Locate every blood parasite and identify its species.
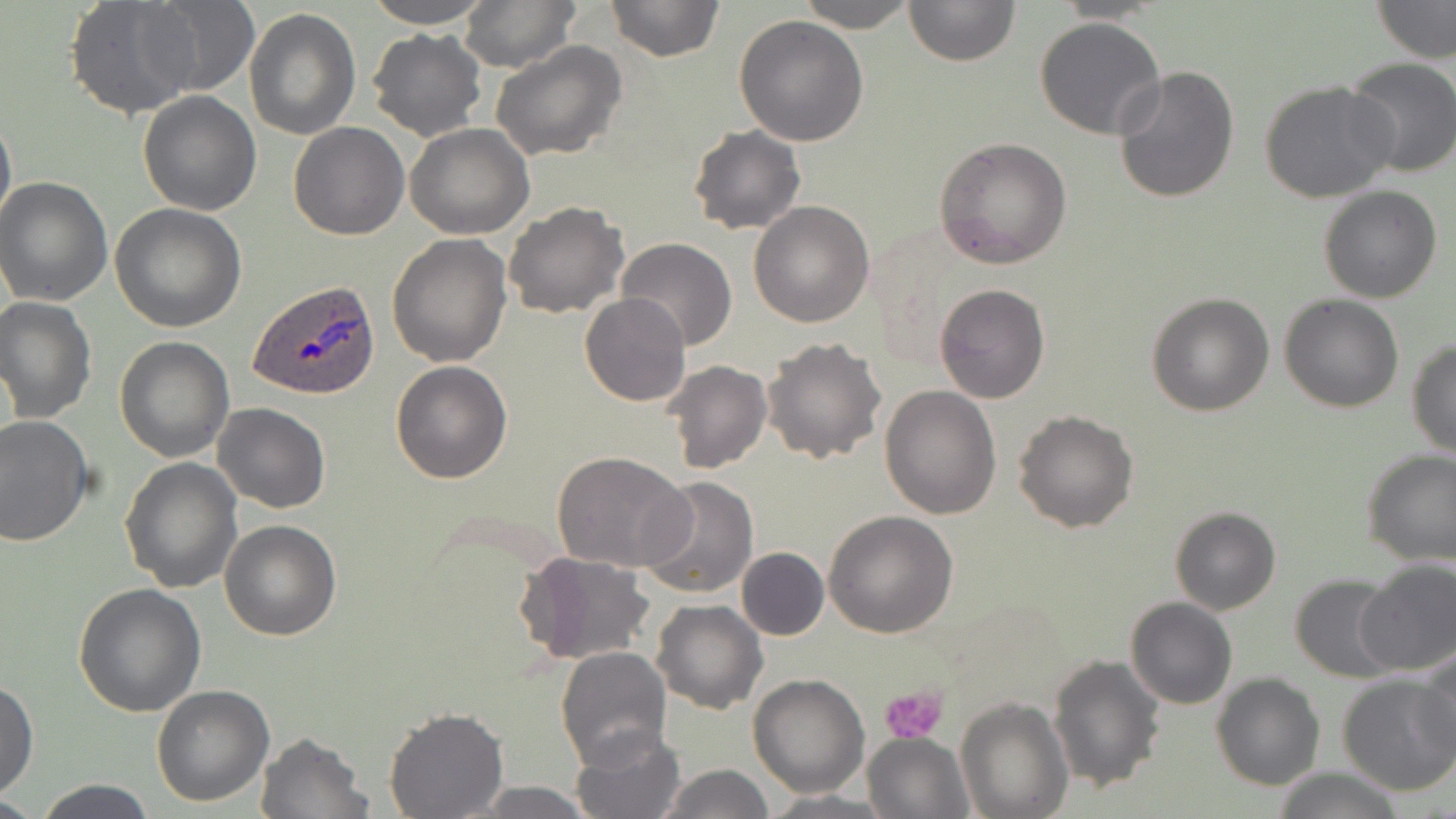
Approximate bounding boxes as (x1,y1)-(x2,y2) corner pairs in pixels.
Plasmodium ovale-infected red blood cells: (249,282)-(380,399).
No Plasmodium falciparum, Plasmodium malariae, Plasmodium vivax, Babesia divergens, or Trypanosoma brucei observed.

Uninfected red blood cell locations: (65,0)-(204,119), (138,0)-(259,96), (360,0)-(496,28), (457,0)-(580,71), (604,0)-(725,63), (797,0)-(915,31), (902,0)-(1019,67), (1371,0)-(1455,64), (244,7)-(360,139), (734,15)-(868,147), (1035,15)-(1167,140), (367,29)-(487,142), (491,40)-(628,162), (1343,57)-(1456,177), (1113,64)-(1240,204), (1259,81)-(1398,205), (137,91)-(261,215), (0,101)-(16,241), (288,122)-(410,240), (405,124)-(534,240), (688,125)-(807,236), (934,136)-(1074,268), (1,175)-(115,306), (1317,184)-(1442,303), (504,200)-(629,319), (748,201)-(875,327), (110,203)-(247,333), (386,233)-(512,368), (616,237)-(736,352), (935,284)-(1050,403), (1146,291)-(1275,416), (579,293)-(692,407), (1279,293)-(1404,412), (0,295)-(98,424), (114,336)-(234,462), (761,336)-(887,464), (1406,339)-(1456,457), (391,360)-(512,483), (663,360)-(772,472), (879,385)-(1002,519), (213,402)-(330,513), (1014,408)-(1140,533), (0,416)-(94,546), (1359,447)-(1456,566), (553,451)-(695,573), (119,456)-(242,593), (639,475)-(759,599), (1169,506)-(1281,615), (824,510)-(959,638), (220,519)-(341,641), (736,547)-(829,639), (516,550)-(655,665), (1357,558)-(1455,675), (1290,574)-(1399,681), (74,584)-(206,717), (1125,597)-(1237,709), (652,601)-(768,715), (556,646)-(671,767), (1416,652)-(1456,768), (1048,653)-(1165,793), (1337,672)-(1455,796), (1210,673)-(1324,790), (747,674)-(872,796), (0,679)-(38,799), (150,684)-(275,806), (955,696)-(1072,818), (385,705)-(507,817), (571,725)-(688,819), (255,731)-(370,819), (863,732)-(973,819), (661,763)-(774,818), (1265,766)-(1405,819), (30,778)-(159,819), (467,781)-(597,817), (759,791)-(892,817). Platelet locations: (880,682)-(950,743). Slide-level diagnosis: Plasmodium ovale. Optical microscopy. Single field of view. May-Grünwald-Giemsa-stained preparation. Thin blood film. 1000x magnification. Image is 1456×819 pixels.